State which parasite is depicted.
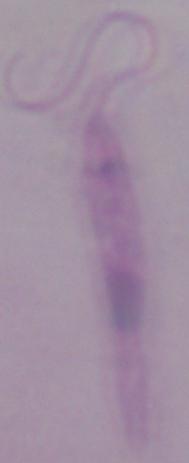
This is Leishmania.

1000x magnification. Micrograph.